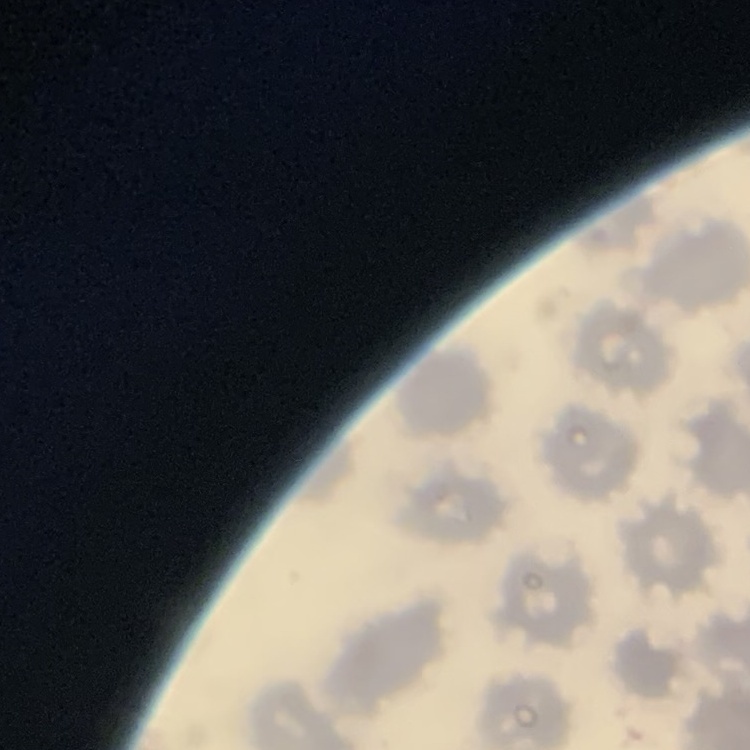

red_blood_cell_morphology: no rouleaux formation
image_type: square crop of a larger photomicrograph
preparation: thin peripheral smear
stain: Field's or Giemsa